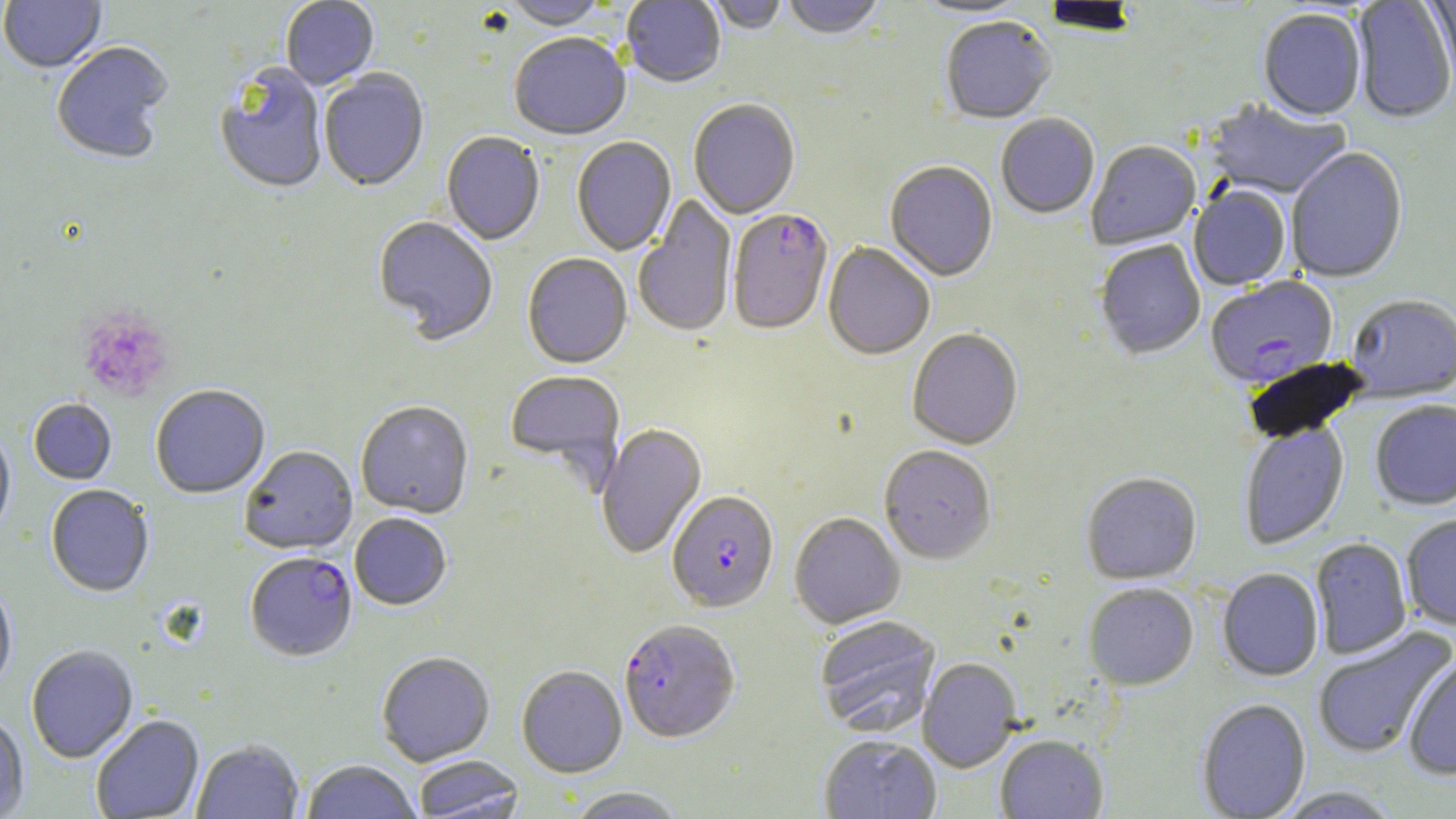
Summary:
  - Coordinate format: approximate bounding boxes as (x1, y1, x2, y2) in pixels
  - Uninfected red blood cell locations: (0, 0, 106, 74), (622, 0, 726, 89), (702, 0, 789, 36), (781, 0, 886, 42), (913, 0, 1032, 20), (1042, 0, 1140, 38), (1352, 0, 1456, 125), (1427, 0, 1456, 94), (281, 1, 380, 91), (503, 1, 607, 32), (1258, 10, 1366, 124), (940, 18, 1056, 126), (509, 35, 630, 142), (51, 43, 174, 165), (215, 64, 328, 196), (320, 70, 429, 193), (688, 100, 800, 221), (1203, 100, 1351, 202), (996, 114, 1100, 220), (441, 132, 545, 246), (572, 138, 676, 256), (1086, 143, 1201, 251), (1286, 149, 1408, 283), (885, 163, 998, 282), (1189, 187, 1291, 291), (633, 196, 736, 338), (372, 217, 498, 345), (1095, 240, 1205, 360), (823, 243, 935, 361), (522, 254, 632, 370), (1347, 297, 1456, 402), (907, 330, 1023, 451), (504, 371, 625, 482), (151, 386, 270, 499), (28, 400, 116, 485), (356, 401, 474, 518), (1370, 401, 1456, 511), (1239, 422, 1350, 551), (596, 424, 707, 559), (0, 428, 16, 542), (239, 446, 358, 556), (879, 446, 997, 565), (1081, 473, 1201, 585), (46, 485, 154, 598), (349, 513, 452, 611), (789, 513, 905, 629), (1401, 513, 1456, 631), (1310, 538, 1412, 660), (1218, 569, 1324, 681), (0, 583, 17, 695), (1083, 583, 1198, 691), (814, 616, 941, 736), (1312, 626, 1455, 760), (26, 645, 139, 764), (376, 651, 495, 767), (1403, 656, 1456, 780), (918, 658, 1022, 773), (517, 665, 628, 778), (1196, 700, 1311, 818), (0, 713, 29, 817), (91, 715, 204, 818), (819, 734, 942, 819), (995, 735, 1108, 819), (191, 739, 304, 819), (413, 756, 525, 818), (300, 760, 420, 819), (565, 787, 687, 818), (1273, 787, 1403, 818)
  - Platelet locations: (77, 308, 176, 402)
  - Plasmodium falciparum-infected red blood cell locations: (728, 210, 833, 336), (1206, 277, 1338, 390), (667, 491, 779, 613), (245, 552, 357, 661), (619, 620, 740, 744)
  - Slide-level diagnosis: Plasmodium falciparum
  - Magnification: 1000x
  - Field of view: single
  - Image size: 1456×819 pixels
  - Stain: May-Grünwald-Giemsa
  - Modality: light microscopy
  - Preparation: thin blood film